Locate every Plasmodium ovale-infected red blood cell.
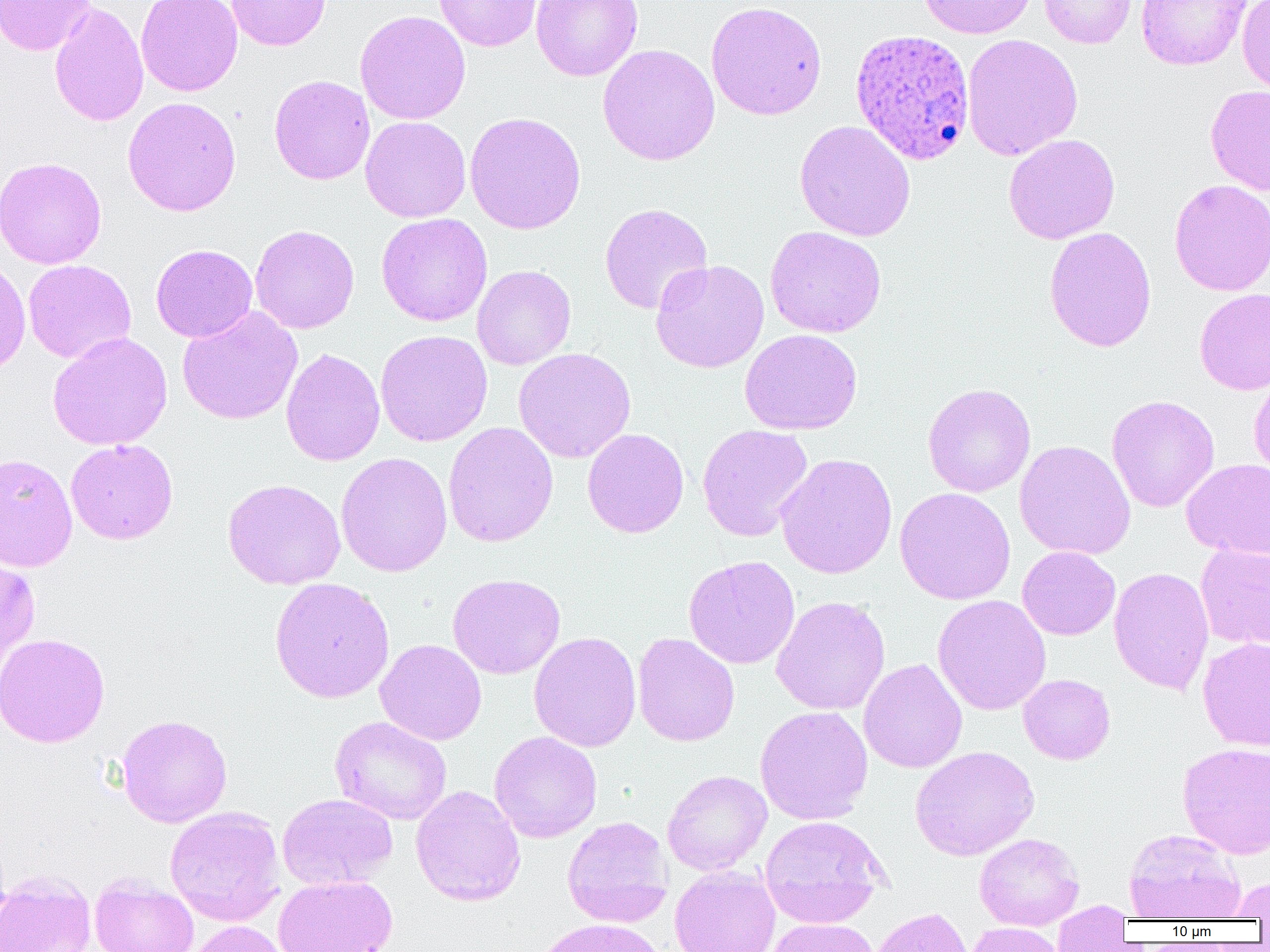
Approximate bounding boxes as [x1, y1, x2, y2] in pixels.
Plasmodium ovale-infected red blood cells: [850, 27, 975, 166].

{
  "slide_level_diagnosis": "Plasmodium ovale",
  "field_of_view": "single",
  "image_size": "1270×952 pixels",
  "preparation": "thin blood film",
  "magnification": "1000x",
  "modality": "light microscopy",
  "uninfected_red_blood_cell_locations": "approximate bounding boxes as [x1, y1, x2, y2] in pixels: [0, 0, 96, 56], [136, 0, 242, 96], [226, 0, 331, 50], [433, 0, 542, 52], [531, 0, 643, 81], [919, 0, 1037, 39], [1038, 0, 1137, 48], [1135, 0, 1252, 70], [1237, 0, 1270, 96], [705, 1, 827, 121], [49, 2, 149, 128], [354, 10, 471, 125], [961, 33, 1083, 161], [597, 43, 720, 166], [269, 74, 375, 185], [1205, 85, 1270, 196], [123, 96, 241, 217], [465, 111, 587, 235], [360, 116, 471, 222], [794, 120, 916, 241], [1003, 133, 1120, 244], [0, 156, 107, 269], [1169, 179, 1270, 296], [599, 203, 713, 314], [376, 213, 492, 327], [250, 224, 359, 334], [765, 226, 886, 338], [1044, 226, 1156, 352], [150, 243, 258, 343], [0, 256, 31, 376], [23, 259, 136, 364], [650, 259, 770, 373], [472, 264, 577, 369], [1195, 287, 1270, 395], [177, 306, 303, 426], [740, 329, 862, 435], [374, 330, 493, 447], [47, 332, 173, 451], [280, 348, 385, 466], [513, 348, 636, 463], [1248, 371, 1270, 481], [922, 383, 1036, 497], [1106, 395, 1219, 513], [443, 421, 559, 548], [697, 424, 814, 542], [582, 428, 689, 538], [66, 439, 178, 544], [1014, 440, 1136, 560], [0, 452, 78, 572], [336, 452, 452, 577], [775, 453, 898, 580], [1182, 458, 1270, 560], [222, 478, 346, 590], [894, 487, 1016, 605], [1195, 543, 1270, 651], [1017, 546, 1120, 640], [0, 554, 41, 672], [683, 555, 801, 669], [1108, 567, 1215, 695], [447, 573, 566, 679], [270, 577, 395, 703], [932, 594, 1051, 715], [770, 596, 890, 715], [528, 631, 642, 752], [632, 632, 740, 747], [0, 633, 110, 748], [375, 638, 487, 746], [1197, 638, 1270, 751], [859, 658, 967, 773], [1018, 674, 1115, 765], [754, 705, 873, 825], [116, 714, 233, 828], [329, 716, 452, 825], [489, 731, 602, 843], [1177, 743, 1270, 859], [910, 746, 1040, 861], [662, 770, 772, 876], [411, 785, 525, 906], [277, 793, 397, 891], [164, 806, 286, 926], [562, 815, 674, 927], [760, 815, 889, 927], [1123, 828, 1245, 921], [974, 832, 1084, 930], [669, 866, 781, 952], [0, 871, 96, 952], [89, 874, 199, 952], [273, 874, 398, 952], [1226, 876, 1270, 920], [1051, 901, 1133, 951], [868, 906, 976, 952], [534, 918, 667, 952], [764, 918, 880, 952], [182, 921, 293, 952], [966, 923, 1067, 952]"
}